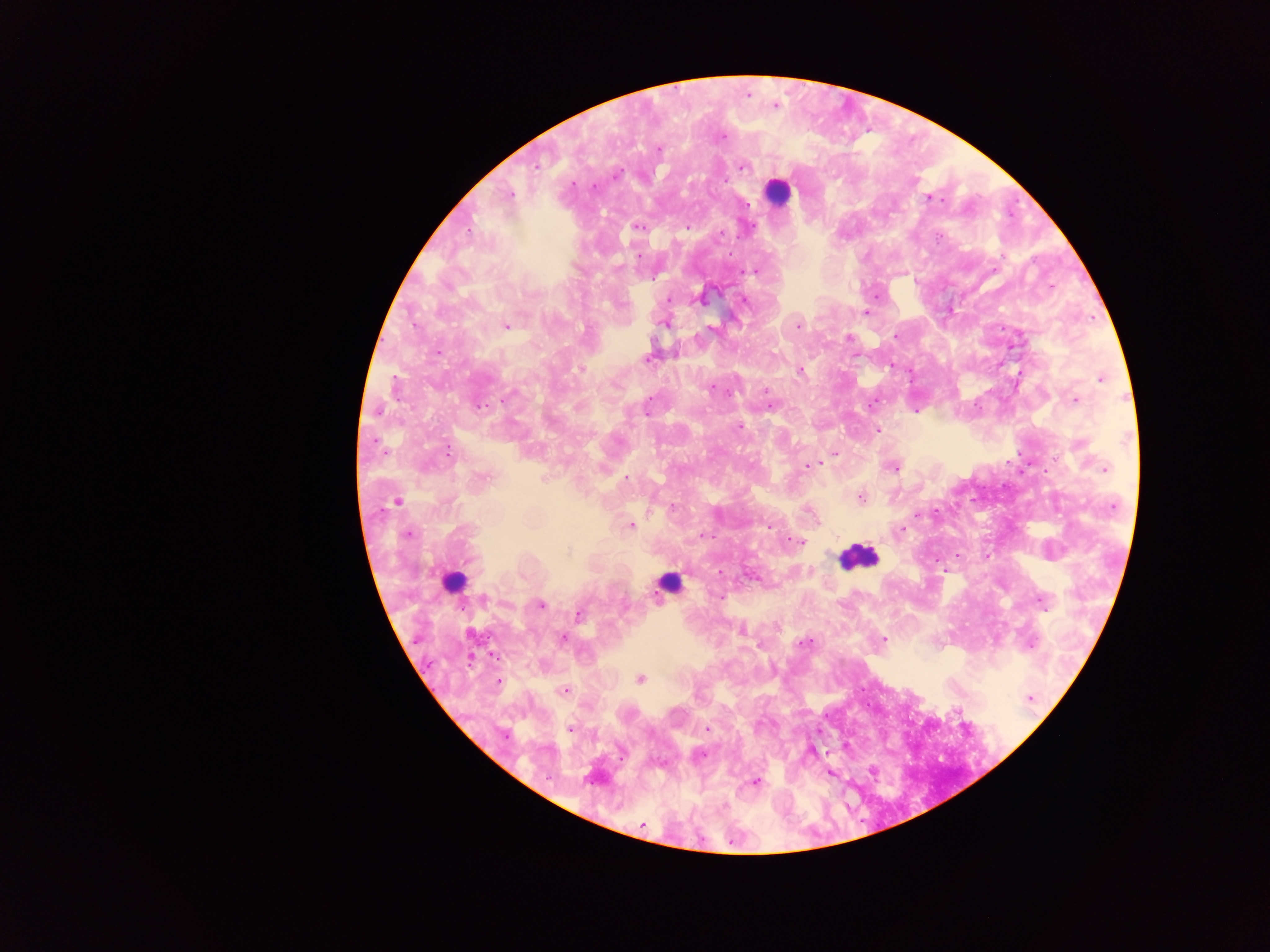
leukocyte locations = approximate centers as (x, y) in pixels: (778, 190), (859, 557), (453, 582), (670, 583)
capture = mobile-phone photograph through a microscope
country = Ghana
field of view = single
Plasmodium parasite locations = approximate centers as (x, y) in pixels: (748, 95), (775, 106), (723, 137), (658, 149), (537, 165), (742, 167), (617, 175), (725, 180), (593, 186), (510, 195), (930, 198), (747, 203), (639, 227), (687, 227), (749, 229), (468, 231), (721, 234), (755, 271), (1051, 287), (702, 298), (669, 299), (744, 300), (866, 313), (664, 323), (506, 326), (797, 326), (712, 328), (895, 335), (849, 337), (438, 352), (646, 359), (581, 368), (800, 370), (1101, 378), (711, 388), (765, 390), (507, 397), (1076, 400), (480, 405), (771, 407), (647, 410), (378, 411), (916, 411), (739, 427), (877, 430), (1080, 445), (447, 452), (835, 453), (808, 466), (894, 468), (1104, 468), (484, 477), (626, 477), (861, 497), (397, 501), (673, 508), (918, 515), (631, 526), (769, 526), (902, 530), (408, 534), (705, 536), (794, 540), (567, 552), (720, 571), (719, 597), (483, 599), (1042, 601), (541, 604), (579, 615), (742, 632), (472, 634), (562, 638), (883, 638), (804, 643), (1031, 644), (640, 679), (499, 682), (565, 690), (1030, 698), (707, 729), (570, 730), (506, 735), (701, 755), (757, 781), (643, 825)
preparation = thick blood smear
image size = 1270×952 pixels